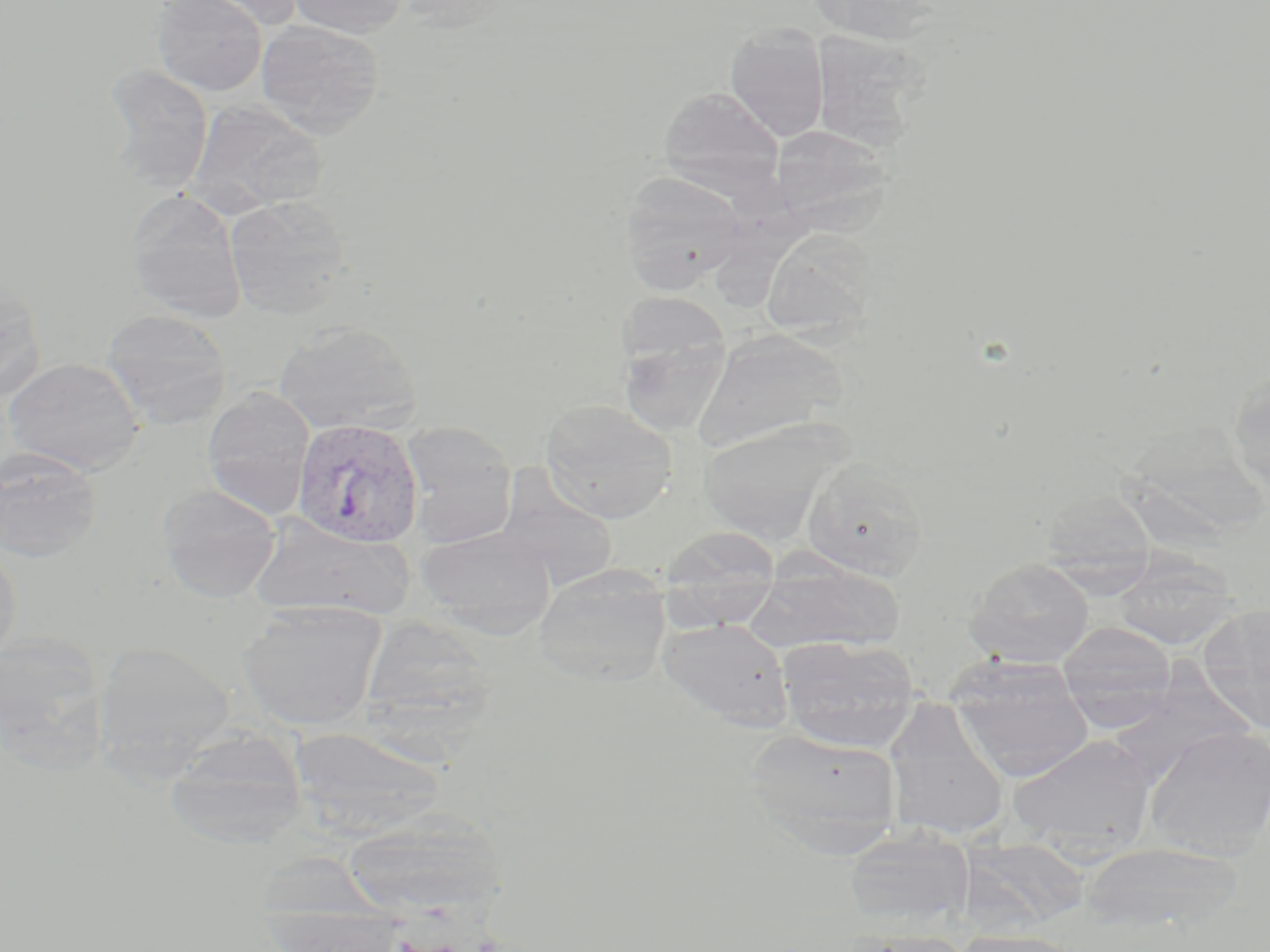 Approximate bounding boxes as (x1, y1, x2, y2) in pixels. Uninfected red blood cell locations: (153, 0, 266, 96), (180, 0, 305, 30), (287, 0, 410, 38), (807, 0, 941, 45), (255, 19, 387, 138), (725, 22, 830, 142), (808, 30, 924, 152), (104, 64, 214, 193), (657, 86, 785, 196), (187, 99, 326, 218), (770, 124, 893, 231), (619, 170, 749, 294), (125, 188, 247, 323), (223, 195, 353, 318), (760, 227, 878, 342), (0, 277, 47, 402), (101, 308, 233, 429), (614, 312, 731, 439), (273, 320, 421, 434), (692, 329, 846, 452), (4, 358, 146, 476), (1228, 368, 1270, 501), (201, 387, 315, 520), (538, 399, 678, 523), (698, 419, 847, 543), (400, 422, 518, 549), (0, 447, 102, 563), (801, 458, 928, 581), (496, 477, 618, 591), (158, 484, 281, 603), (1039, 488, 1158, 589), (247, 514, 414, 622), (658, 525, 782, 622), (417, 526, 556, 636), (0, 542, 21, 666), (1109, 555, 1240, 649), (966, 558, 1095, 667), (747, 559, 905, 654), (532, 565, 672, 687), (238, 599, 389, 731), (1198, 602, 1270, 732), (360, 616, 498, 739), (657, 616, 794, 730), (1057, 621, 1177, 729), (0, 632, 111, 771), (776, 635, 922, 752), (93, 642, 235, 781), (949, 664, 1095, 782), (882, 704, 1009, 843), (1142, 725, 1270, 861), (288, 726, 446, 839), (164, 727, 308, 851), (744, 728, 902, 855), (1007, 734, 1157, 855), (342, 807, 506, 917), (842, 829, 975, 929), (959, 838, 1090, 931), (1078, 841, 1244, 935), (265, 906, 410, 951), (844, 929, 975, 952), (952, 930, 1089, 952). Plasmodium vivax-infected red blood cell locations: (292, 420, 425, 549). Slide-level diagnosis: Plasmodium vivax. Image is 1270×952 pixels. Captured at 1000x magnification. May-Grünwald-Giemsa stain. Thin blood smear. One field of a larger specimen. Light microscopy.